Classify this cell by malaria status.
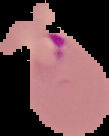
Parasitized.

Image is 109×136 pixels. From a thin blood film. Segmented cell region on a black background.